Assess this cell for malaria.
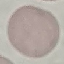

Uninfected.

preparation = thin blood smear
capture = smartphone camera at the microscope eyepiece
stain = Giemsa
image type = cell patch, automatically extracted from a larger field of view and resized to 64 × 64 pixels